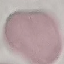

{
  "malaria_status": "uninfected",
  "stain": "Giemsa",
  "capture": "smartphone camera at the microscope eyepiece",
  "preparation": "thin blood film",
  "image_type": "automatically extracted cell patch, resized to 64 × 64 pixels"
}